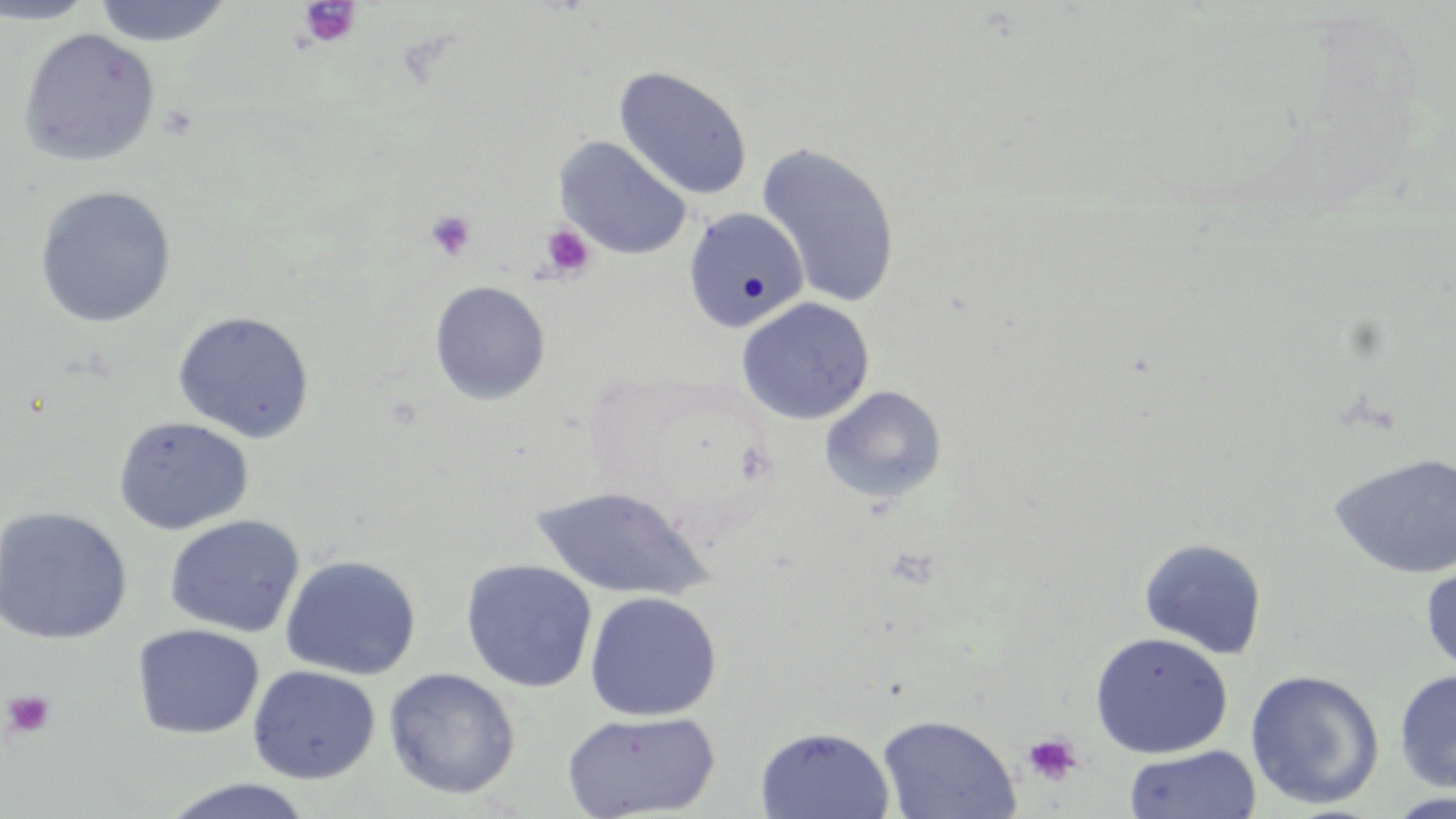

Summary:
  - Coordinate format: approximate bounding boxes as (x1, y1, x2, y2) in pixels
  - Uninfected red blood cell locations: (0, 0, 100, 26), (91, 0, 234, 47), (18, 28, 160, 166), (614, 66, 753, 201), (555, 137, 692, 261), (756, 142, 902, 309), (34, 186, 177, 328), (682, 208, 809, 332), (429, 280, 550, 406), (735, 297, 875, 425), (172, 310, 315, 443), (819, 385, 947, 504), (112, 415, 254, 535), (1328, 451, 1456, 580), (532, 485, 711, 601), (0, 507, 133, 646), (164, 515, 304, 638), (1138, 536, 1268, 659), (280, 554, 421, 680), (460, 559, 597, 692), (1420, 560, 1456, 678), (584, 591, 722, 721), (132, 624, 265, 739), (1090, 631, 1232, 758), (247, 665, 380, 784), (383, 668, 521, 799), (1245, 669, 1384, 810), (1394, 669, 1456, 793), (561, 710, 720, 819), (877, 715, 1021, 819), (755, 725, 895, 819), (1124, 745, 1262, 819), (158, 778, 319, 819), (1384, 792, 1456, 819)
  - Platelet locations: (297, 1, 361, 48), (425, 209, 477, 261), (540, 224, 594, 279), (2, 689, 56, 738), (1022, 732, 1083, 787)
  - Slide-level diagnosis: negative for blood parasites
  - Modality: light microscopy
  - Stain: May-Grünwald-Giemsa
  - Field of view: single
  - Image size: 1456×819 pixels
  - Magnification: 1000x
  - Preparation: thin blood smear